Locate and identify every blood parasite.
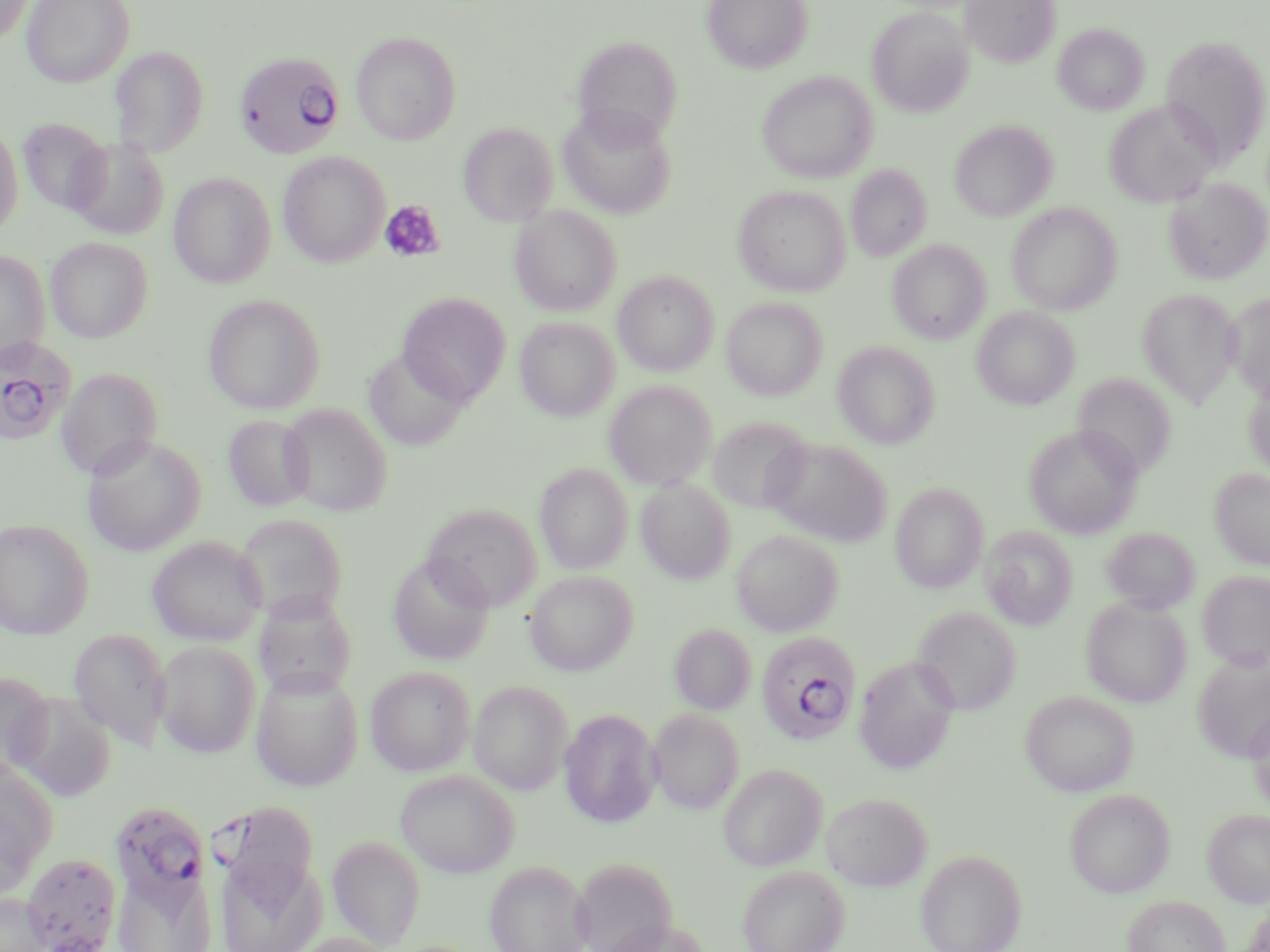

Approximate bounding boxes as named x1/y1/x2/y2 corners in pixels.
Plasmodium falciparum-infected red blood cells: (x1=233, y1=52, x2=345, y2=160), (x1=0, y1=337, x2=77, y2=445), (x1=756, y1=632, x2=861, y2=746), (x1=205, y1=801, x2=318, y2=926), (x1=108, y1=804, x2=215, y2=926), (x1=22, y1=851, x2=121, y2=951).
No Plasmodium ovale, Plasmodium malariae, Plasmodium vivax, Babesia divergens, or Trypanosoma brucei observed.

Platelet locations: (x1=379, y1=200, x2=447, y2=264). Uninfected red blood cell locations: (x1=0, y1=0, x2=31, y2=44), (x1=22, y1=0, x2=135, y2=88), (x1=703, y1=0, x2=812, y2=73), (x1=962, y1=0, x2=1060, y2=67), (x1=867, y1=8, x2=972, y2=117), (x1=1053, y1=24, x2=1149, y2=115), (x1=352, y1=32, x2=461, y2=145), (x1=1159, y1=34, x2=1270, y2=169), (x1=572, y1=36, x2=683, y2=144), (x1=111, y1=45, x2=209, y2=156), (x1=758, y1=71, x2=877, y2=183), (x1=1104, y1=100, x2=1220, y2=208), (x1=557, y1=104, x2=676, y2=219), (x1=18, y1=118, x2=111, y2=215), (x1=950, y1=119, x2=1056, y2=222), (x1=458, y1=122, x2=558, y2=226), (x1=0, y1=123, x2=22, y2=240), (x1=66, y1=138, x2=169, y2=239), (x1=278, y1=151, x2=389, y2=267), (x1=846, y1=164, x2=932, y2=262), (x1=168, y1=173, x2=276, y2=288), (x1=1164, y1=177, x2=1269, y2=284), (x1=733, y1=185, x2=850, y2=296), (x1=1006, y1=203, x2=1122, y2=315), (x1=510, y1=205, x2=622, y2=316), (x1=46, y1=237, x2=154, y2=343), (x1=888, y1=239, x2=990, y2=344), (x1=0, y1=251, x2=50, y2=365), (x1=613, y1=271, x2=718, y2=376), (x1=1138, y1=290, x2=1242, y2=407), (x1=1226, y1=292, x2=1270, y2=403), (x1=204, y1=293, x2=325, y2=413), (x1=397, y1=293, x2=511, y2=405), (x1=722, y1=298, x2=827, y2=400), (x1=972, y1=307, x2=1079, y2=409), (x1=514, y1=316, x2=620, y2=421), (x1=833, y1=341, x2=940, y2=448), (x1=364, y1=348, x2=471, y2=450), (x1=56, y1=368, x2=164, y2=479), (x1=1073, y1=372, x2=1176, y2=479), (x1=604, y1=380, x2=717, y2=489), (x1=1244, y1=380, x2=1270, y2=477), (x1=279, y1=403, x2=392, y2=516), (x1=223, y1=414, x2=314, y2=511), (x1=708, y1=417, x2=814, y2=515), (x1=1024, y1=423, x2=1142, y2=538), (x1=82, y1=435, x2=206, y2=556), (x1=764, y1=439, x2=891, y2=547), (x1=535, y1=463, x2=633, y2=574), (x1=1209, y1=468, x2=1270, y2=570), (x1=636, y1=478, x2=735, y2=583), (x1=890, y1=482, x2=989, y2=592), (x1=421, y1=502, x2=543, y2=611), (x1=234, y1=514, x2=347, y2=623), (x1=0, y1=518, x2=94, y2=638), (x1=980, y1=526, x2=1077, y2=629), (x1=1101, y1=527, x2=1200, y2=613), (x1=732, y1=529, x2=844, y2=636), (x1=147, y1=536, x2=266, y2=645), (x1=388, y1=554, x2=495, y2=665), (x1=525, y1=570, x2=638, y2=676), (x1=1197, y1=571, x2=1270, y2=670), (x1=253, y1=594, x2=357, y2=699), (x1=1081, y1=597, x2=1192, y2=707), (x1=912, y1=606, x2=1020, y2=715), (x1=670, y1=624, x2=756, y2=715), (x1=68, y1=628, x2=173, y2=752), (x1=154, y1=641, x2=261, y2=758), (x1=1192, y1=650, x2=1270, y2=763), (x1=853, y1=656, x2=959, y2=773), (x1=366, y1=665, x2=476, y2=776), (x1=251, y1=667, x2=364, y2=790), (x1=0, y1=671, x2=55, y2=782), (x1=469, y1=679, x2=573, y2=794), (x1=1020, y1=690, x2=1138, y2=796), (x1=8, y1=693, x2=117, y2=802), (x1=1246, y1=704, x2=1270, y2=814), (x1=560, y1=709, x2=661, y2=827), (x1=649, y1=709, x2=745, y2=812), (x1=0, y1=762, x2=59, y2=880), (x1=718, y1=763, x2=827, y2=871), (x1=395, y1=769, x2=520, y2=877), (x1=1064, y1=788, x2=1176, y2=898), (x1=821, y1=791, x2=932, y2=891), (x1=0, y1=796, x2=39, y2=905), (x1=1202, y1=808, x2=1270, y2=907), (x1=328, y1=835, x2=426, y2=949), (x1=915, y1=849, x2=1027, y2=952), (x1=215, y1=850, x2=327, y2=952), (x1=570, y1=856, x2=677, y2=952), (x1=484, y1=859, x2=592, y2=952), (x1=737, y1=865, x2=849, y2=952), (x1=112, y1=866, x2=216, y2=952), (x1=1, y1=891, x2=54, y2=952), (x1=1122, y1=895, x2=1230, y2=952), (x1=602, y1=918, x2=714, y2=952), (x1=289, y1=932, x2=401, y2=952). Slide-level diagnosis: Plasmodium falciparum. One field of a larger specimen. May-Grünwald-Giemsa stain. Thin blood film. Captured at 1000x magnification. Optical microscopy. Image is 1270×952 pixels.